Identify the cell.
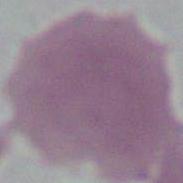

This is an erythrocyte.

Summary:
  - Modality: photomicrograph
  - Magnification: 1000x